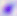

Summary:
  - Modality: micrograph
  - Identification: Toxoplasma gondii
  - Magnification: 400x